Outline each blood parasite and name the species.
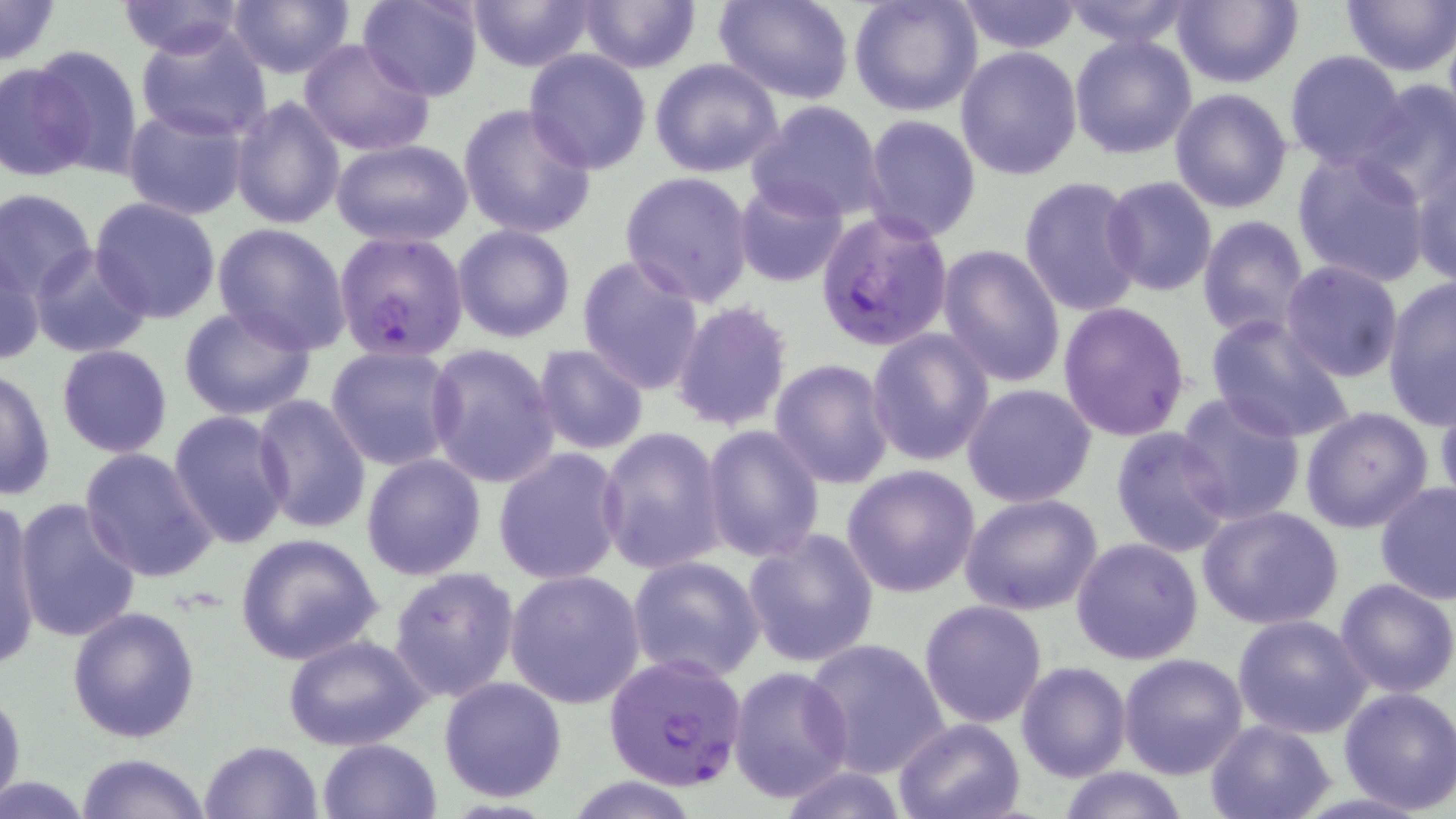
Approximate bounding boxes as named x1/y1/x2/y2 corners in pixels.
Plasmodium falciparum-infected red blood cells: (x1=814, y1=209, x2=954, y2=351), (x1=332, y1=230, x2=469, y2=360), (x1=602, y1=653, x2=753, y2=791).
No Plasmodium ovale, Plasmodium malariae, Plasmodium vivax, Babesia divergens, or Trypanosoma brucei observed.

Uninfected red blood cell locations: (x1=0, y1=0, x2=63, y2=66), (x1=225, y1=0, x2=355, y2=78), (x1=357, y1=0, x2=483, y2=101), (x1=462, y1=0, x2=599, y2=71), (x1=578, y1=0, x2=702, y2=72), (x1=714, y1=0, x2=855, y2=103), (x1=849, y1=0, x2=984, y2=118), (x1=1057, y1=0, x2=1200, y2=49), (x1=1170, y1=0, x2=1301, y2=89), (x1=116, y1=1, x2=249, y2=58), (x1=955, y1=1, x2=1084, y2=53), (x1=1340, y1=1, x2=1456, y2=76), (x1=136, y1=22, x2=272, y2=143), (x1=1069, y1=32, x2=1198, y2=159), (x1=298, y1=38, x2=433, y2=157), (x1=25, y1=44, x2=145, y2=179), (x1=954, y1=46, x2=1083, y2=180), (x1=523, y1=49, x2=653, y2=173), (x1=1283, y1=50, x2=1408, y2=169), (x1=649, y1=57, x2=783, y2=177), (x1=0, y1=59, x2=95, y2=181), (x1=1350, y1=80, x2=1456, y2=207), (x1=1169, y1=87, x2=1292, y2=213), (x1=229, y1=95, x2=345, y2=230), (x1=747, y1=99, x2=887, y2=224), (x1=458, y1=104, x2=597, y2=240), (x1=120, y1=105, x2=251, y2=221), (x1=862, y1=114, x2=981, y2=240), (x1=331, y1=138, x2=474, y2=247), (x1=1291, y1=148, x2=1431, y2=287), (x1=1412, y1=155, x2=1456, y2=288), (x1=621, y1=171, x2=754, y2=306), (x1=1018, y1=176, x2=1146, y2=317), (x1=1101, y1=176, x2=1218, y2=297), (x1=733, y1=178, x2=850, y2=288), (x1=1084, y1=182, x2=1209, y2=409), (x1=0, y1=188, x2=97, y2=298), (x1=90, y1=197, x2=222, y2=322), (x1=1196, y1=215, x2=1311, y2=340), (x1=213, y1=224, x2=350, y2=352), (x1=451, y1=224, x2=576, y2=344), (x1=937, y1=244, x2=1066, y2=389), (x1=29, y1=245, x2=153, y2=358), (x1=1, y1=248, x2=46, y2=369), (x1=576, y1=255, x2=706, y2=396), (x1=1279, y1=261, x2=1405, y2=384), (x1=1382, y1=276, x2=1455, y2=428), (x1=670, y1=300, x2=796, y2=434), (x1=1058, y1=300, x2=1190, y2=440), (x1=177, y1=304, x2=317, y2=420), (x1=1204, y1=312, x2=1355, y2=444), (x1=866, y1=328, x2=996, y2=468), (x1=425, y1=342, x2=560, y2=488), (x1=57, y1=344, x2=172, y2=458), (x1=325, y1=344, x2=459, y2=472), (x1=532, y1=344, x2=650, y2=454), (x1=769, y1=359, x2=895, y2=488), (x1=1, y1=367, x2=56, y2=501), (x1=960, y1=383, x2=1099, y2=508), (x1=1434, y1=387, x2=1456, y2=512), (x1=1175, y1=392, x2=1307, y2=526), (x1=251, y1=395, x2=372, y2=534), (x1=1300, y1=406, x2=1435, y2=534), (x1=167, y1=410, x2=292, y2=550), (x1=700, y1=424, x2=824, y2=564), (x1=597, y1=427, x2=728, y2=577), (x1=1110, y1=427, x2=1236, y2=558), (x1=78, y1=446, x2=219, y2=583), (x1=493, y1=448, x2=625, y2=585), (x1=362, y1=454, x2=485, y2=581), (x1=842, y1=464, x2=983, y2=597), (x1=1373, y1=481, x2=1456, y2=605), (x1=960, y1=493, x2=1104, y2=616), (x1=1, y1=495, x2=45, y2=670), (x1=12, y1=499, x2=143, y2=643), (x1=1198, y1=505, x2=1345, y2=631), (x1=742, y1=528, x2=879, y2=669), (x1=233, y1=532, x2=383, y2=666), (x1=1070, y1=537, x2=1204, y2=665), (x1=626, y1=555, x2=767, y2=683), (x1=388, y1=567, x2=522, y2=704), (x1=504, y1=570, x2=646, y2=708), (x1=1334, y1=577, x2=1455, y2=698), (x1=919, y1=600, x2=1049, y2=729), (x1=68, y1=606, x2=201, y2=743), (x1=1233, y1=614, x2=1370, y2=738), (x1=283, y1=635, x2=431, y2=752), (x1=803, y1=637, x2=951, y2=779), (x1=1119, y1=652, x2=1248, y2=778), (x1=1016, y1=661, x2=1132, y2=783), (x1=728, y1=665, x2=855, y2=802), (x1=439, y1=675, x2=568, y2=803), (x1=0, y1=685, x2=25, y2=815), (x1=1335, y1=685, x2=1456, y2=813), (x1=893, y1=717, x2=1025, y2=819), (x1=1204, y1=718, x2=1334, y2=819), (x1=318, y1=738, x2=442, y2=819), (x1=199, y1=739, x2=324, y2=819), (x1=75, y1=753, x2=211, y2=819), (x1=770, y1=766, x2=913, y2=819), (x1=1055, y1=766, x2=1191, y2=819), (x1=561, y1=777, x2=705, y2=817). Slide-level diagnosis: Plasmodium falciparum. May-Grünwald-Giemsa-stained preparation. Image is 1456×819 pixels. Light microscopy. Thin blood smear. One field of a larger specimen. 1000x magnification.